State which parasite is depicted.
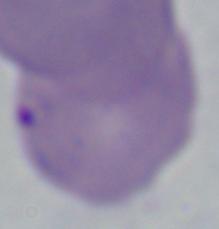

Babesia.

1000x magnification. Micrograph.